Outline each blood parasite and name the species.
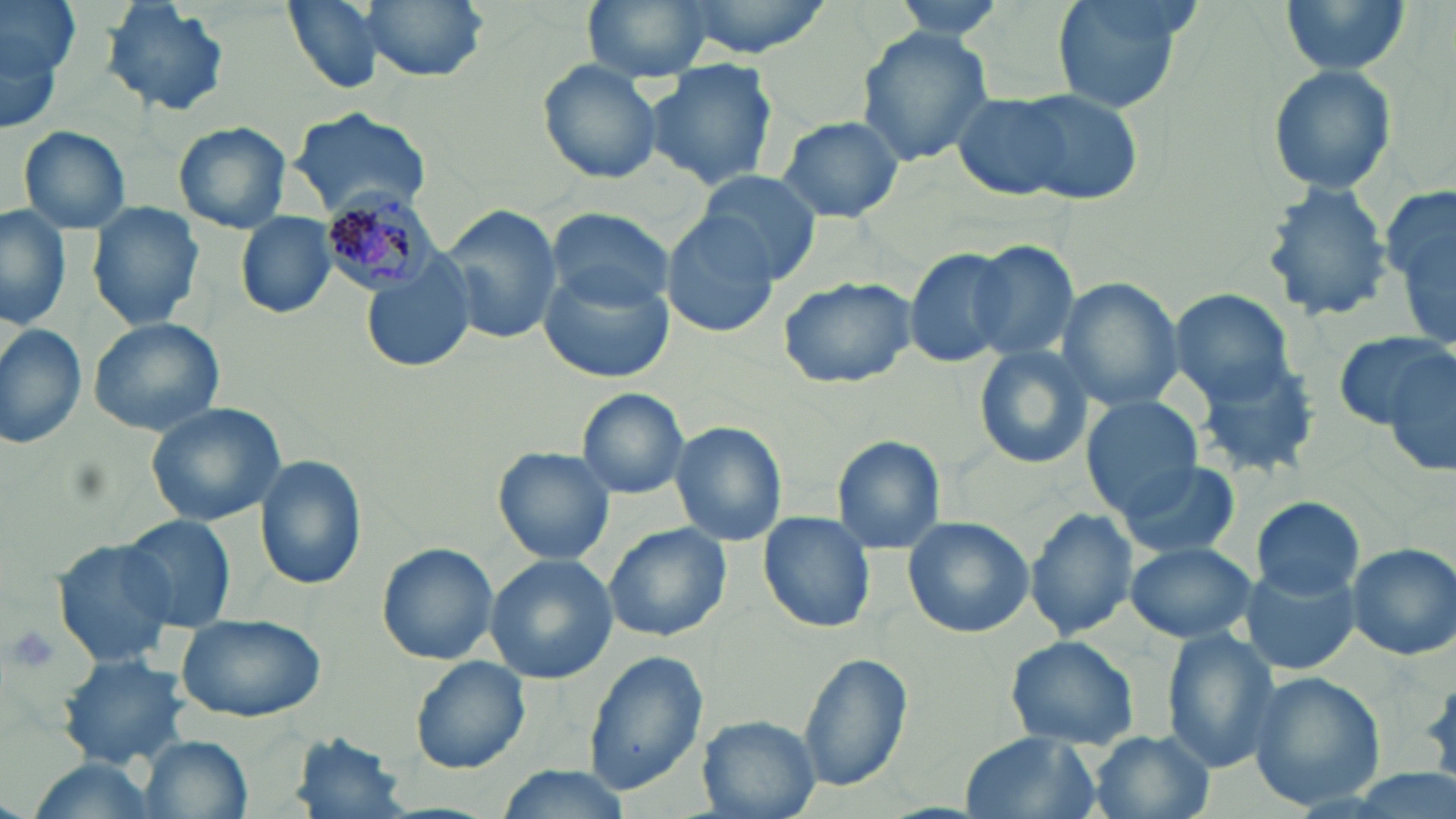
Approximate bounding boxes as (x1, y1, x2, y2) in pixels.
Plasmodium malariae-infected red blood cells: (318, 177, 437, 299).
No Plasmodium falciparum, Plasmodium ovale, Plasmodium vivax, Babesia divergens, or Trypanosoma brucei observed.

slide-level diagnosis = Plasmodium malariae
stain = May-Grünwald-Giemsa
field of view = one of a larger specimen
modality = light microscopy
magnification = 1000x
platelet locations = approximate bounding boxes as (x1, y1, x2, y2) in pixels: (5, 623, 65, 678)
preparation = thin blood smear
uninfected red blood cell locations = approximate bounding boxes as (x1, y1, x2, y2) in pixels: (0, 0, 78, 108), (101, 0, 229, 116), (280, 0, 395, 94), (356, 0, 487, 82), (581, 0, 714, 83), (664, 0, 840, 60), (885, 0, 1010, 39), (1051, 0, 1193, 112), (1280, 0, 1411, 78), (853, 25, 995, 166), (536, 59, 665, 184), (647, 60, 779, 191), (1266, 63, 1398, 197), (950, 92, 1089, 199), (1012, 92, 1144, 205), (286, 108, 432, 218), (775, 114, 904, 223), (172, 121, 293, 234), (17, 125, 132, 235), (696, 170, 824, 281), (1259, 182, 1394, 326), (1379, 182, 1456, 345), (86, 203, 205, 331), (441, 204, 562, 344), (0, 205, 71, 331), (546, 206, 676, 313), (660, 211, 778, 337), (236, 212, 335, 318), (966, 238, 1080, 361), (906, 247, 1018, 369), (360, 257, 476, 376), (538, 262, 678, 383), (776, 277, 916, 390), (1056, 279, 1183, 412), (1169, 288, 1298, 406), (87, 316, 225, 436), (0, 322, 87, 450), (1336, 329, 1452, 433), (1376, 338, 1456, 480), (972, 345, 1095, 470), (1191, 355, 1323, 481), (575, 388, 691, 501), (1080, 393, 1204, 517), (144, 401, 287, 527), (670, 421, 787, 547), (830, 435, 947, 556), (495, 447, 616, 565), (256, 456, 367, 591), (1115, 458, 1240, 560), (1250, 495, 1364, 600), (1025, 507, 1137, 641), (759, 510, 875, 633), (118, 514, 236, 633), (902, 516, 1034, 638), (602, 522, 731, 644), (52, 537, 179, 668), (376, 541, 499, 666), (1123, 541, 1256, 644), (1347, 542, 1456, 662), (485, 555, 618, 684), (1242, 559, 1361, 676), (173, 612, 330, 725), (1160, 630, 1281, 772), (1005, 635, 1141, 749), (583, 650, 705, 792), (797, 652, 913, 795), (56, 654, 191, 768), (409, 655, 531, 774), (1245, 673, 1386, 810), (697, 716, 818, 817), (956, 730, 1099, 819), (1087, 730, 1214, 819), (291, 732, 410, 818), (139, 734, 253, 819), (21, 756, 162, 819), (490, 765, 631, 819)
image size = 1456×819 pixels